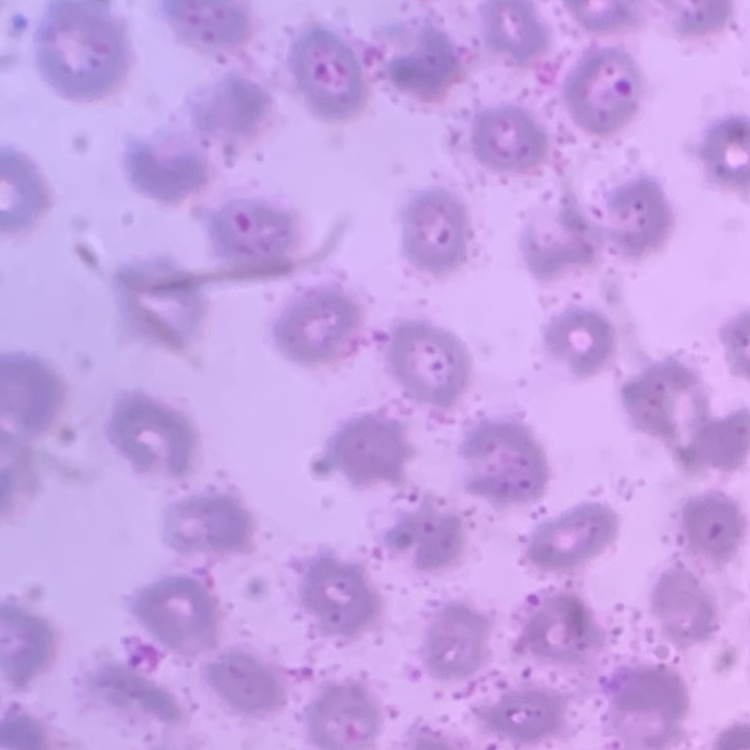
red_blood_cell_morphology: no rouleaux formation
image_type: one tile cut from a larger photomicrograph
stain: Field's or Giemsa
preparation: thin peripheral smear